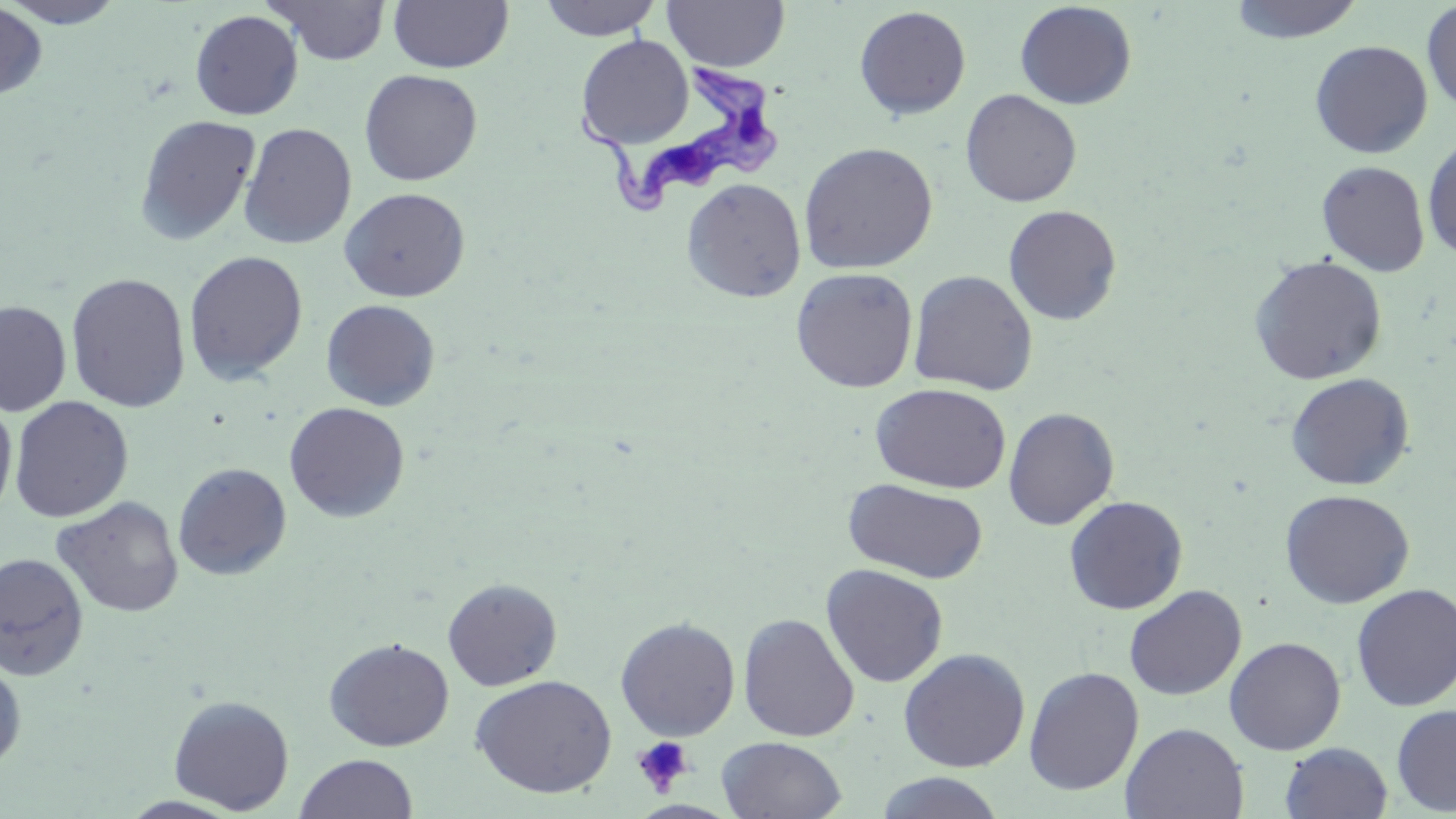
Summary:
  - Coordinate format: approximate bounding boxes as named x1/y1/x2/y2 corners in pixels
  - Uninfected red blood cell locations: (x1=1, y1=0, x2=128, y2=28), (x1=388, y1=0, x2=513, y2=73), (x1=538, y1=0, x2=662, y2=40), (x1=663, y1=0, x2=789, y2=72), (x1=1227, y1=0, x2=1366, y2=44), (x1=266, y1=1, x2=392, y2=65), (x1=1015, y1=1, x2=1137, y2=110), (x1=1421, y1=2, x2=1455, y2=117), (x1=0, y1=3, x2=46, y2=101), (x1=853, y1=5, x2=971, y2=120), (x1=190, y1=9, x2=303, y2=120), (x1=576, y1=34, x2=693, y2=149), (x1=1309, y1=40, x2=1432, y2=159), (x1=359, y1=69, x2=483, y2=186), (x1=960, y1=89, x2=1082, y2=207), (x1=134, y1=114, x2=261, y2=246), (x1=239, y1=122, x2=357, y2=250), (x1=1422, y1=134, x2=1456, y2=261), (x1=799, y1=141, x2=938, y2=274), (x1=1316, y1=160, x2=1430, y2=276), (x1=681, y1=178, x2=806, y2=302), (x1=339, y1=187, x2=470, y2=302), (x1=1003, y1=204, x2=1122, y2=326), (x1=184, y1=250, x2=308, y2=385), (x1=1248, y1=255, x2=1388, y2=385), (x1=791, y1=267, x2=918, y2=393), (x1=908, y1=270, x2=1038, y2=396), (x1=66, y1=272, x2=191, y2=413), (x1=321, y1=299, x2=441, y2=411), (x1=0, y1=300, x2=72, y2=416), (x1=1285, y1=373, x2=1414, y2=490), (x1=872, y1=383, x2=1011, y2=494), (x1=9, y1=396, x2=134, y2=523), (x1=0, y1=398, x2=17, y2=521), (x1=284, y1=402, x2=410, y2=523), (x1=1003, y1=407, x2=1119, y2=530), (x1=173, y1=462, x2=292, y2=581), (x1=842, y1=478, x2=989, y2=584), (x1=1279, y1=489, x2=1415, y2=608), (x1=1064, y1=495, x2=1188, y2=615), (x1=52, y1=497, x2=184, y2=618), (x1=0, y1=553, x2=90, y2=681), (x1=821, y1=564, x2=949, y2=688), (x1=442, y1=578, x2=563, y2=691), (x1=1124, y1=584, x2=1247, y2=701), (x1=1351, y1=584, x2=1456, y2=712), (x1=738, y1=613, x2=860, y2=742), (x1=614, y1=616, x2=741, y2=741), (x1=1224, y1=636, x2=1346, y2=755), (x1=324, y1=637, x2=454, y2=751), (x1=898, y1=647, x2=1031, y2=772), (x1=0, y1=657, x2=27, y2=774), (x1=1023, y1=666, x2=1144, y2=796), (x1=470, y1=674, x2=616, y2=798), (x1=168, y1=694, x2=294, y2=815), (x1=1391, y1=704, x2=1456, y2=815), (x1=1120, y1=723, x2=1249, y2=818), (x1=717, y1=736, x2=847, y2=819), (x1=1280, y1=742, x2=1393, y2=818), (x1=294, y1=754, x2=418, y2=819), (x1=874, y1=772, x2=1006, y2=818)
  - Trypanosoma brucei locations: (x1=570, y1=59, x2=787, y2=216)
  - Platelet locations: (x1=632, y1=736, x2=694, y2=796)
  - Slide-level diagnosis: Trypanosoma brucei
  - Image size: 1456×819 pixels
  - Preparation: thin blood smear
  - Modality: optical microscopy
  - Magnification: 1000x
  - Field of view: single
  - Stain: May-Grünwald-Giemsa